Classify this cell by malaria status.
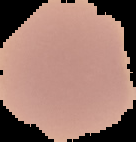
It is uninfected.

From a thin blood smear. Image is 136×142 pixels. The area outside the segmented cell region is set to black.